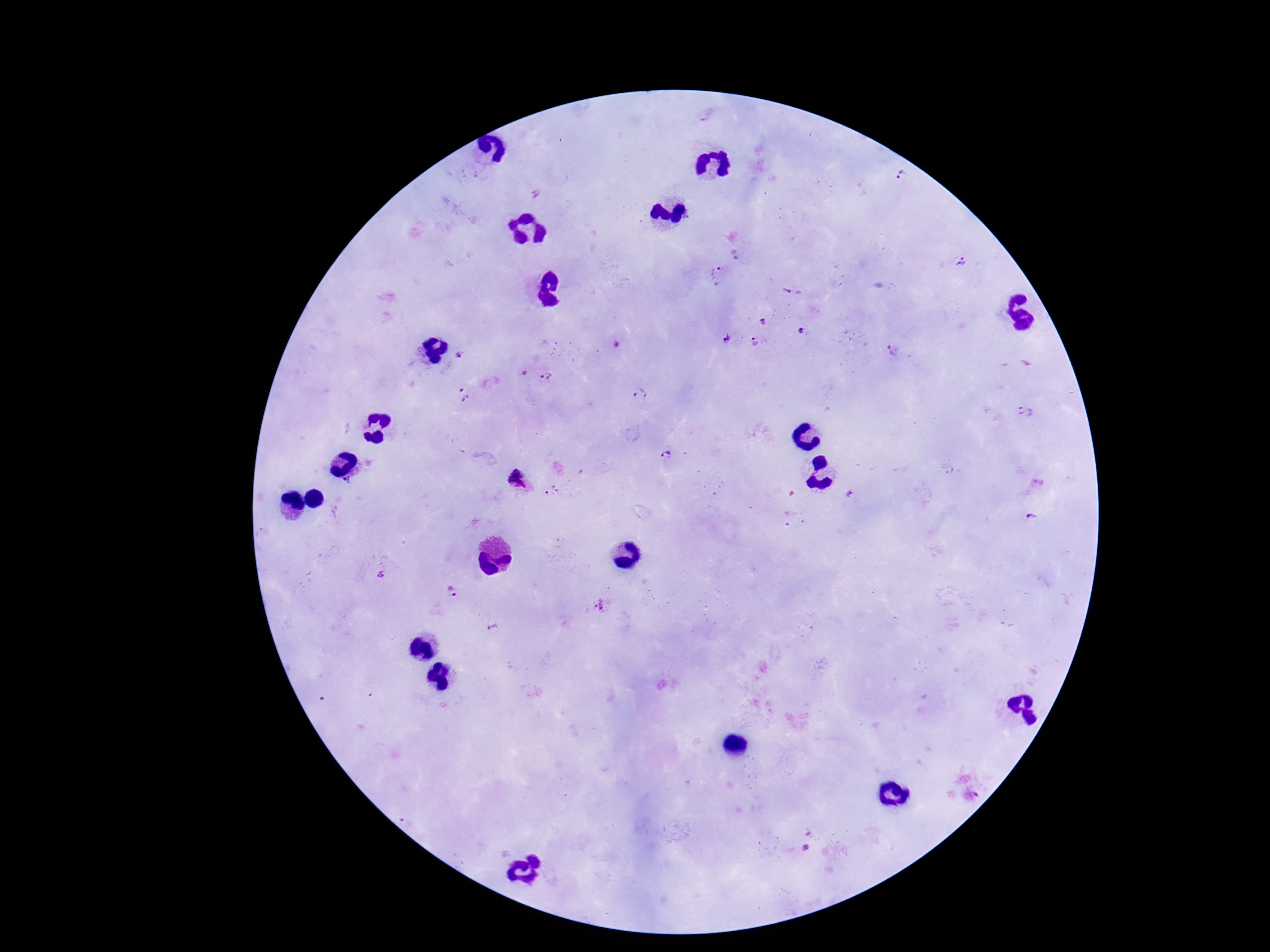

Approximate centers as {x, y} in pixels. Plasmodium parasite locations: {903, 177}, {534, 195}, {737, 252}, {960, 262}, {717, 276}, {792, 292}, {764, 320}, {800, 330}, {726, 337}, {754, 341}, {893, 353}, {460, 355}, {545, 377}, {640, 392}, {462, 395}, {1027, 413}, {666, 456}, {518, 477}, {347, 481}, {1039, 483}, {551, 491}, {850, 494}, {1033, 519}, {377, 574}, {453, 591}, {601, 604}, {492, 628}. Smartphone photograph taken through the microscope eyepiece. Thick peripheral-blood smear. 100x magnification. Patient malaria status: infected. Image is 1270×952 pixels. Giemsa stain. One field from this slide.